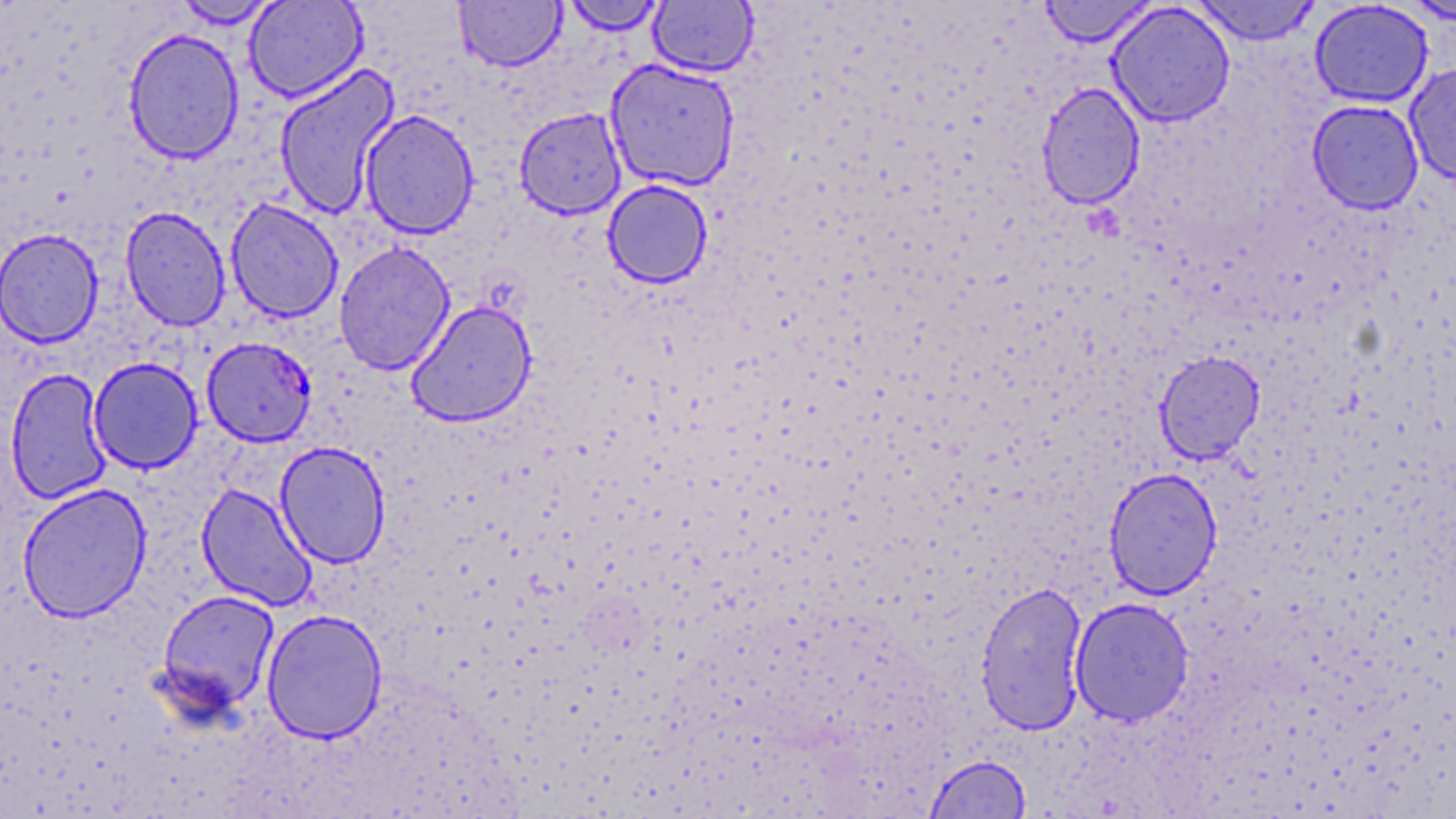

{
  "slide_level_diagnosis": "Plasmodium falciparum",
  "magnification": "1000x",
  "preparation": "thin blood film",
  "image_size": "1456×819 pixels",
  "uninfected_red_blood_cell_locations": "approximate bounding boxes as [x1, y1, x2, y2] in pixels: [173, 0, 282, 29], [243, 0, 368, 102], [453, 0, 566, 73], [562, 0, 667, 35], [1038, 0, 1157, 47], [1190, 0, 1322, 45], [1402, 0, 1456, 26], [648, 1, 759, 77], [1309, 1, 1434, 108], [1107, 2, 1236, 127], [123, 27, 245, 165], [604, 58, 741, 192], [274, 63, 401, 220], [1404, 63, 1456, 184], [1036, 82, 1146, 210], [1307, 99, 1424, 214], [514, 107, 627, 219], [359, 109, 479, 240], [602, 180, 713, 288], [225, 198, 344, 324], [119, 206, 231, 332], [0, 228, 103, 348], [333, 241, 455, 375], [405, 299, 537, 427], [1154, 350, 1266, 464], [87, 357, 203, 474], [5, 367, 113, 504], [275, 441, 392, 568], [1103, 467, 1223, 600], [16, 482, 153, 623], [196, 482, 317, 611], [974, 580, 1089, 736], [156, 589, 281, 716], [1069, 597, 1195, 726], [261, 608, 387, 744], [925, 754, 1032, 818]",
  "plasmodium_falciparum_infected_red_blood_cell_locations": "approximate bounding boxes as [x1, y1, x2, y2] in pixels: [201, 336, 317, 447]",
  "modality": "light microscopy",
  "field_of_view": "single",
  "stain": "May-Grünwald-Giemsa"
}